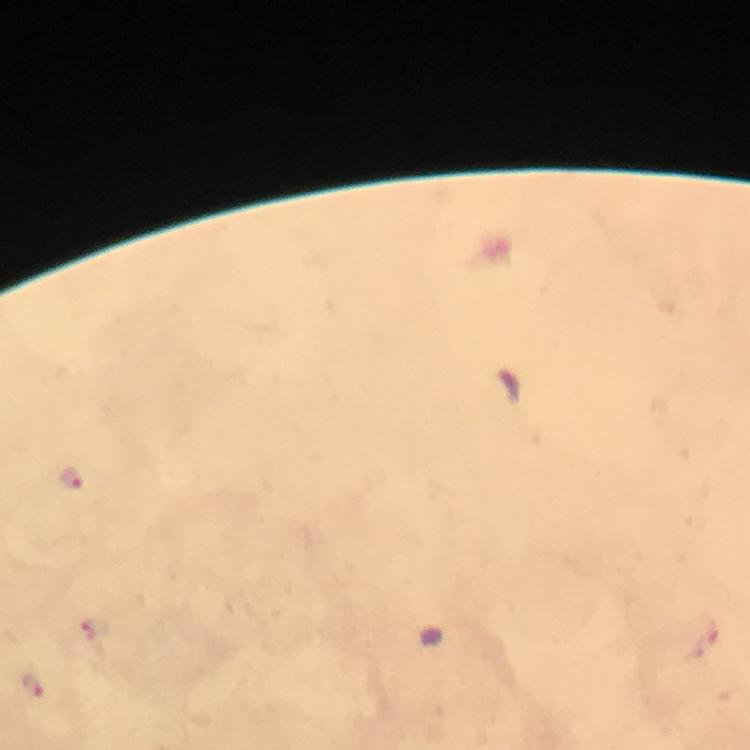

magnification = 100x
capture = smartphone mounted on the microscope
image size = 750×750 pixels
context = from a diagnostic examination for malaria
stain = Giemsa
preparation = thick blood film
malaria parasite locations = approximate centers as {x, y} in pixels: {68, 478}, {92, 627}, {35, 684}
cropped from = a single field of view
immersion oil = applied